Give the location of every parasitized red blood cell.
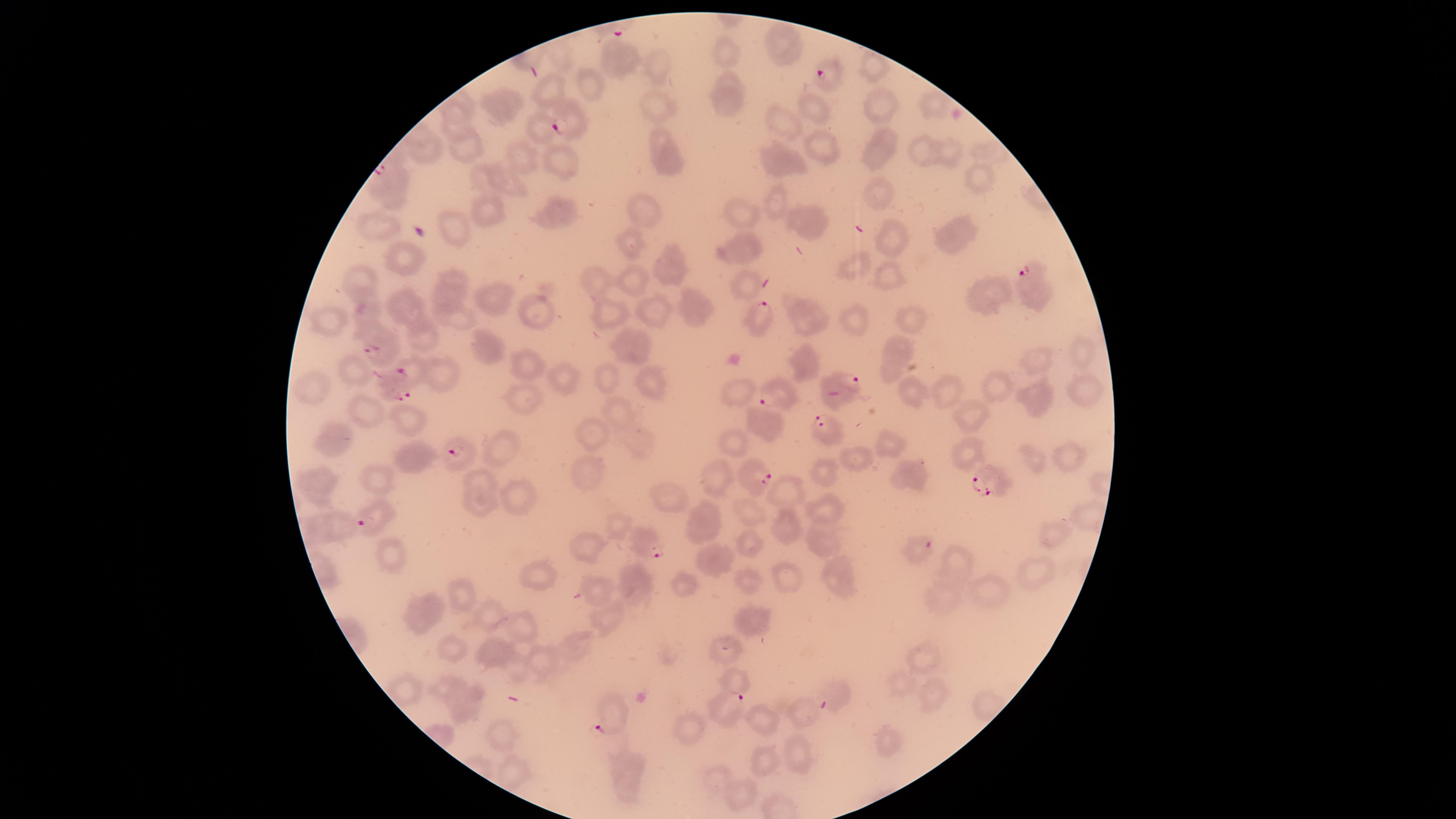

Approximate marker points, in pixels from the top-left corner.
Parasitized red blood cells: (x=825, y=71), (x=566, y=117), (x=1024, y=277), (x=755, y=311), (x=374, y=342), (x=410, y=370), (x=847, y=387), (x=392, y=392), (x=762, y=397), (x=823, y=429), (x=459, y=453), (x=758, y=472), (x=983, y=482), (x=376, y=518), (x=645, y=541), (x=728, y=706), (x=607, y=708).

Approximate marker points, in pixels from the top-left corner. Uninfected red blood cells: (x=781, y=36), (x=725, y=52), (x=560, y=55), (x=620, y=59), (x=660, y=65), (x=872, y=66), (x=590, y=81), (x=548, y=89), (x=730, y=91), (x=654, y=102), (x=877, y=102), (x=815, y=103), (x=501, y=104), (x=931, y=107), (x=454, y=116), (x=785, y=122), (x=535, y=128), (x=463, y=139), (x=822, y=145), (x=421, y=149), (x=883, y=149), (x=667, y=152), (x=923, y=152), (x=945, y=152), (x=526, y=161), (x=562, y=162), (x=783, y=162), (x=981, y=173), (x=477, y=178), (x=506, y=185), (x=880, y=191), (x=777, y=203), (x=490, y=212), (x=644, y=212), (x=553, y=213), (x=740, y=215), (x=802, y=220), (x=374, y=227), (x=455, y=229), (x=957, y=234), (x=891, y=240), (x=631, y=242), (x=748, y=246), (x=402, y=257), (x=669, y=262), (x=854, y=268), (x=885, y=273), (x=365, y=274), (x=457, y=276), (x=635, y=277), (x=596, y=278), (x=746, y=284), (x=447, y=294), (x=403, y=296), (x=497, y=298), (x=993, y=298), (x=366, y=306), (x=693, y=306), (x=533, y=309), (x=610, y=310), (x=651, y=310), (x=800, y=314), (x=456, y=317), (x=853, y=318), (x=912, y=318), (x=328, y=320), (x=425, y=336), (x=626, y=344), (x=490, y=348), (x=899, y=354), (x=1077, y=354), (x=808, y=358), (x=1036, y=361), (x=521, y=364), (x=359, y=369), (x=606, y=376), (x=443, y=378), (x=566, y=378), (x=646, y=379), (x=311, y=382), (x=999, y=385), (x=1084, y=386), (x=945, y=390), (x=738, y=393), (x=1037, y=393), (x=527, y=394), (x=913, y=394), (x=620, y=410), (x=363, y=413), (x=405, y=413), (x=973, y=415), (x=765, y=424), (x=593, y=432), (x=635, y=436), (x=335, y=443), (x=506, y=444), (x=737, y=446), (x=888, y=446), (x=969, y=456), (x=1062, y=456), (x=413, y=457), (x=1032, y=457), (x=856, y=460), (x=822, y=471), (x=583, y=473), (x=908, y=473), (x=375, y=476), (x=483, y=478), (x=720, y=479), (x=317, y=482), (x=778, y=487), (x=518, y=491), (x=670, y=500), (x=478, y=501), (x=818, y=508), (x=746, y=509), (x=1085, y=515), (x=708, y=517), (x=328, y=521), (x=783, y=524), (x=1048, y=535), (x=815, y=536), (x=749, y=541), (x=591, y=546), (x=914, y=552), (x=392, y=555), (x=720, y=559), (x=959, y=564), (x=1033, y=569), (x=839, y=572), (x=539, y=575), (x=746, y=577), (x=786, y=578), (x=633, y=579), (x=684, y=582), (x=993, y=587), (x=594, y=589), (x=945, y=593), (x=464, y=596), (x=426, y=610), (x=491, y=615), (x=760, y=616), (x=607, y=620), (x=520, y=622), (x=452, y=647), (x=727, y=648), (x=492, y=651), (x=576, y=651), (x=545, y=657), (x=922, y=658), (x=733, y=680), (x=449, y=684), (x=904, y=686), (x=932, y=689), (x=838, y=693), (x=465, y=710), (x=800, y=713), (x=762, y=719), (x=688, y=725), (x=883, y=741), (x=795, y=753), (x=764, y=759), (x=628, y=775), (x=743, y=793). Circular visible region. Smartphone photograph through the microscope eyepiece. Image is 1456×819 pixels. One field of view of the specimen. Giemsa stain. Species: Plasmodium falciparum. Thin blood smear.